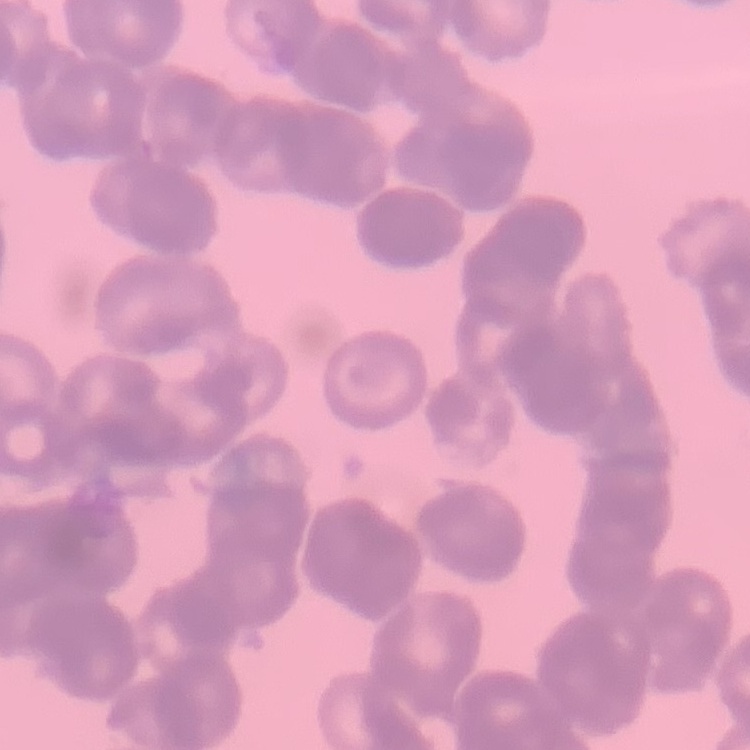
The erythrocytes exhibit rouleaux formation. Thin blood smear. Field's or Giemsa stain. Square crop of a larger photomicrograph.